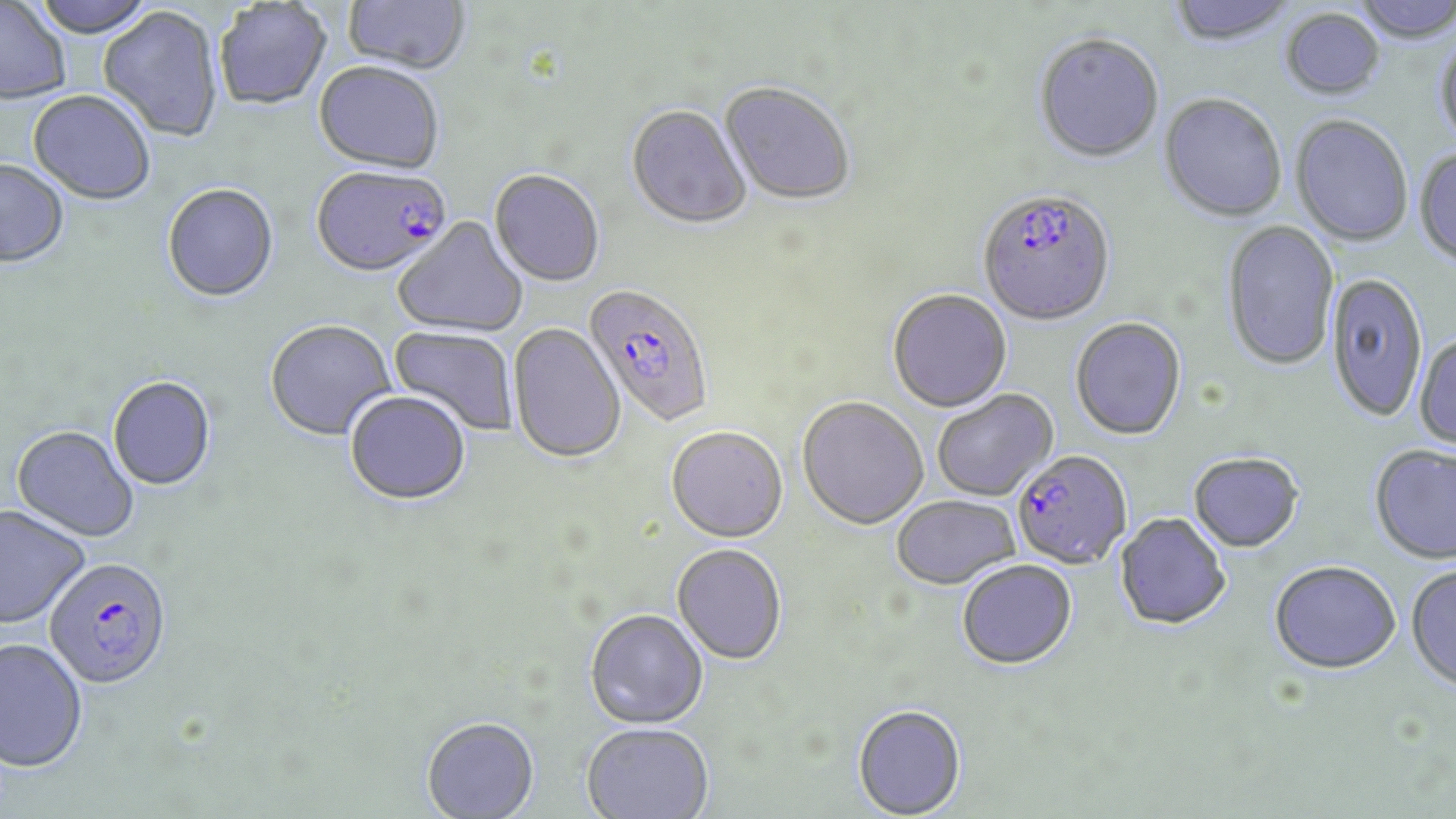 Approximate bounding boxes as [x1, y1, x2, y2] in pixels. Uninfected red blood cell locations: [31, 0, 158, 39], [343, 0, 471, 75], [1167, 0, 1298, 48], [1350, 0, 1456, 45], [0, 2, 72, 105], [214, 2, 332, 111], [98, 7, 223, 143], [1281, 9, 1385, 101], [1435, 32, 1456, 149], [1032, 34, 1164, 164], [313, 63, 444, 175], [719, 83, 856, 207], [27, 91, 156, 206], [1159, 95, 1287, 223], [626, 106, 752, 231], [1290, 116, 1413, 247], [1414, 148, 1456, 269], [0, 160, 69, 268], [489, 169, 605, 288], [162, 184, 279, 304], [392, 218, 529, 339], [1222, 220, 1339, 372], [1327, 274, 1428, 424], [887, 290, 1012, 413], [1070, 318, 1187, 441], [265, 320, 397, 442], [508, 323, 626, 465], [388, 325, 520, 438], [1413, 334, 1456, 452], [108, 377, 216, 491], [932, 390, 1058, 501], [344, 391, 472, 505], [797, 398, 928, 530], [11, 426, 139, 542], [665, 428, 788, 544], [1369, 445, 1456, 565], [1188, 452, 1304, 553], [891, 495, 1021, 589], [0, 504, 90, 629], [1115, 513, 1231, 630], [672, 544, 788, 666], [957, 559, 1077, 670], [1269, 561, 1401, 673], [1406, 564, 1456, 692], [584, 610, 708, 729], [0, 638, 89, 771], [852, 704, 967, 819], [421, 716, 540, 818], [581, 723, 714, 819]. Plasmodium falciparum-infected red blood cell locations: [311, 166, 453, 280], [977, 191, 1116, 328], [583, 284, 715, 427], [1012, 451, 1131, 571], [43, 557, 172, 689]. Slide-level diagnosis: Plasmodium falciparum. May-Grünwald-Giemsa-stained preparation. Image is 1456×819 pixels. 1000x magnification. Optical microscopy. Thin blood smear. One field of a larger specimen.